Identify the cell.
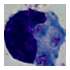
A leukocyte.

Summary:
  - Modality: photomicrograph
  - Magnification: 1000x